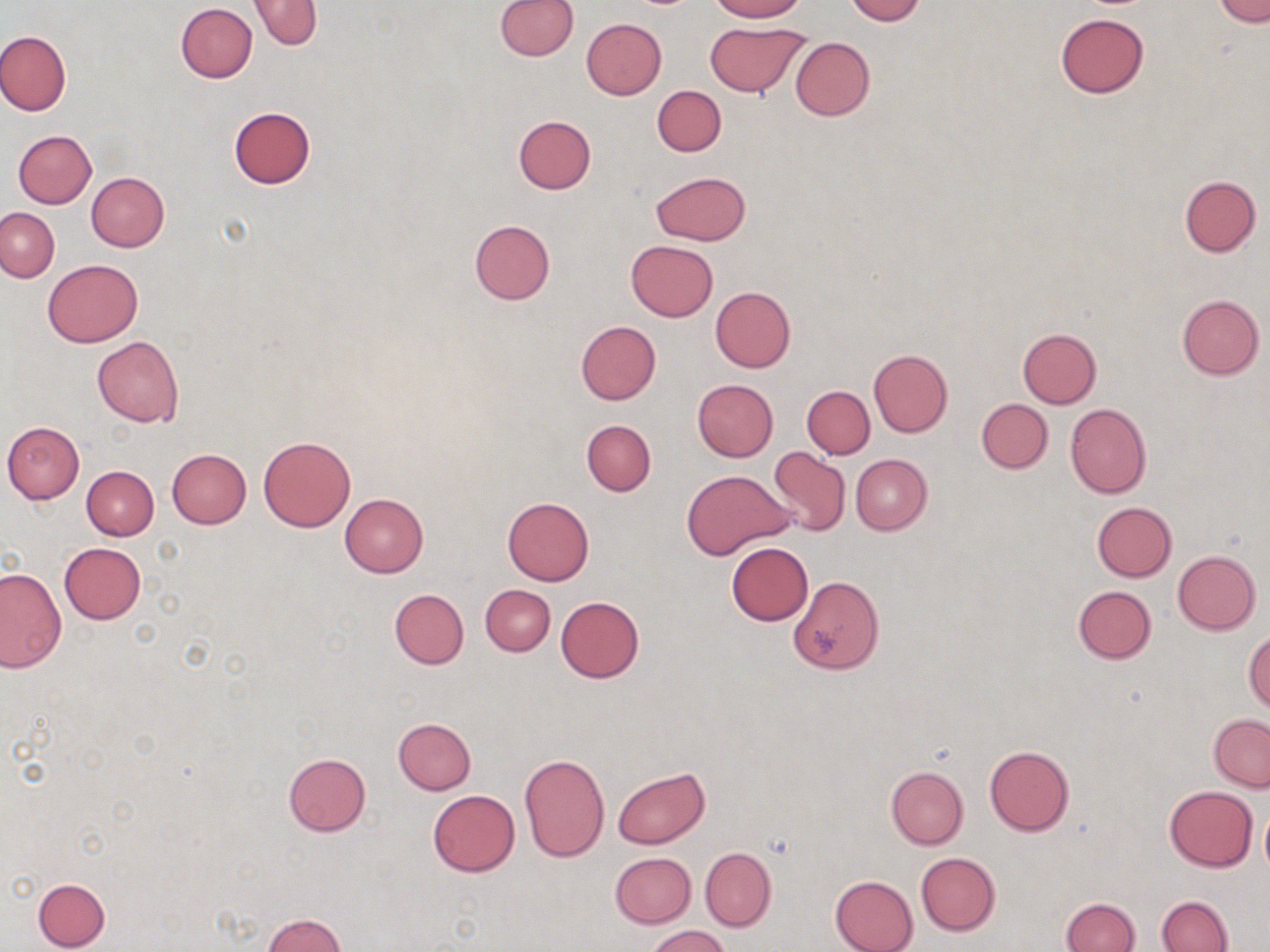

slide-level diagnosis = negative for blood parasites
uninfected red blood cell locations = approximate bounding boxes as (x1,y1)-(x2,y2) corner pairs in pixels: (495,0)-(577,60), (707,0)-(807,22), (846,0)-(924,24), (1215,0)-(1269,26), (249,1)-(322,49), (176,4)-(258,82), (1055,13)-(1148,98), (582,18)-(666,99), (703,21)-(809,97), (0,30)-(72,116), (789,37)-(874,121), (652,85)-(726,156), (227,107)-(316,189), (513,115)-(595,194), (12,130)-(97,208), (651,171)-(750,246), (86,173)-(169,251), (1179,176)-(1260,256), (0,208)-(59,282), (469,219)-(555,305), (625,239)-(718,321), (43,259)-(142,346), (709,286)-(795,372), (1176,295)-(1264,380), (575,320)-(661,404), (1017,328)-(1100,408), (91,336)-(184,426), (868,349)-(952,437), (691,378)-(778,462), (802,386)-(875,459), (976,399)-(1052,473), (1065,403)-(1151,498), (582,419)-(656,496), (2,421)-(85,504), (258,436)-(355,532), (768,447)-(851,536), (167,448)-(252,528), (850,454)-(932,535), (82,466)-(159,540), (681,468)-(792,559), (340,493)-(429,577), (502,496)-(595,585), (1091,501)-(1177,581), (58,542)-(146,624), (725,542)-(814,625), (1172,550)-(1261,634), (0,567)-(66,673), (787,575)-(884,674), (481,584)-(555,656), (1073,586)-(1156,663), (390,589)-(469,669), (556,596)-(644,683), (1245,632)-(1270,714), (1208,714)-(1270,791), (392,717)-(476,794), (984,746)-(1074,835), (282,753)-(371,835), (519,753)-(609,861), (613,766)-(710,849), (886,766)-(968,849), (1164,785)-(1257,872), (428,790)-(519,877), (1260,806)-(1270,877), (700,847)-(776,932), (915,851)-(1000,936), (611,852)-(696,927), (829,864)-(1000,944), (829,875)-(919,952), (33,877)-(111,950), (1157,896)-(1232,952), (1061,898)-(1139,952), (262,913)-(346,951), (645,925)-(730,952)
image size = 1270×952 pixels
magnification = 1000x
stain = May-Grünwald-Giemsa
field of view = single
modality = light microscopy
preparation = thin blood film